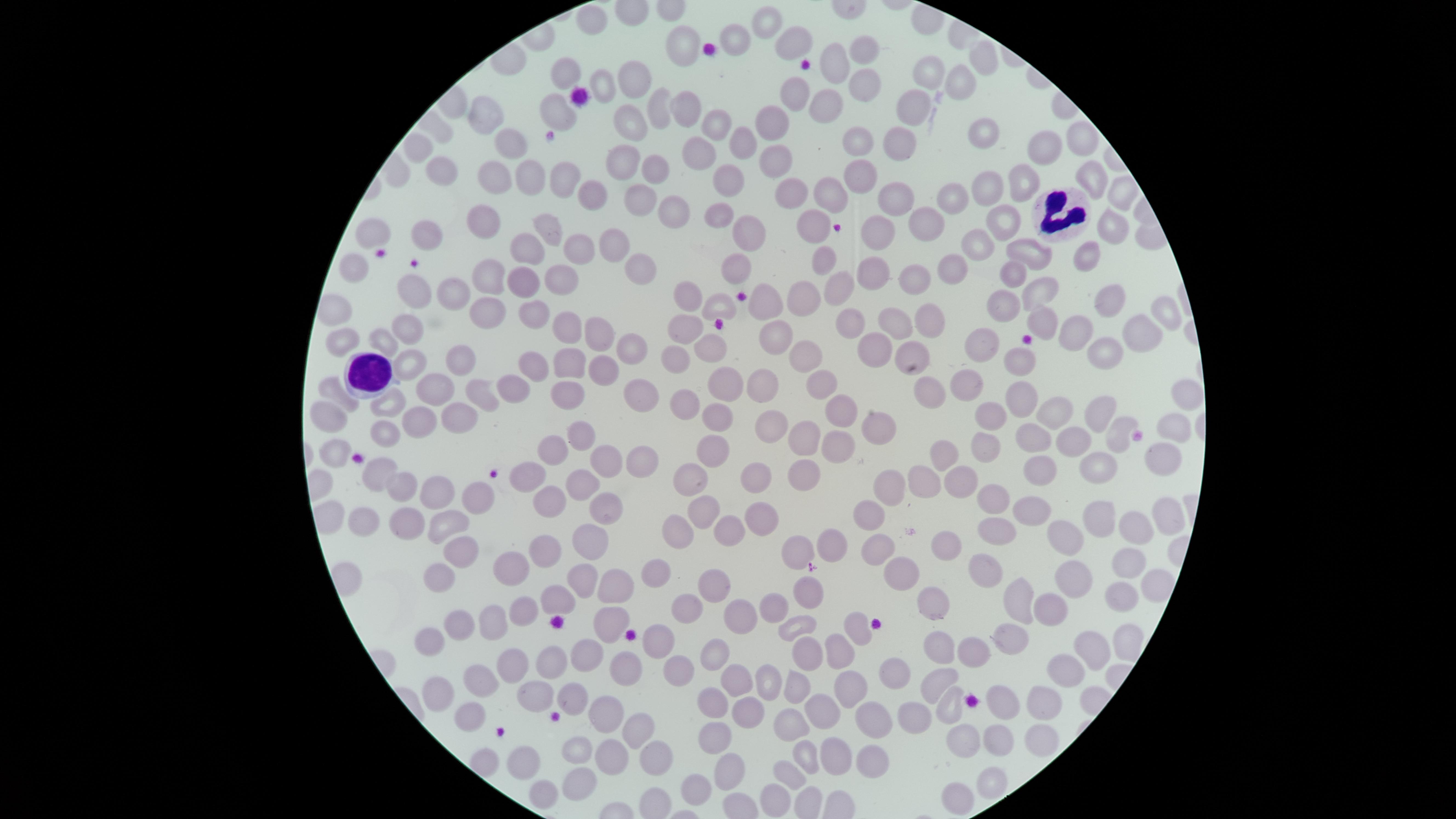
Approximate marker points as {x, y} in pixels. WBCs: {1062, 216}, {365, 371}. Uninfected RBCs: {593, 23}, {767, 26}, {736, 34}, {680, 40}, {793, 41}, {864, 44}, {983, 56}, {835, 63}, {564, 71}, {928, 74}, {633, 77}, {958, 80}, {863, 82}, {604, 87}, {793, 91}, {911, 102}, {658, 103}, {827, 106}, {684, 110}, {556, 113}, {490, 114}, {717, 122}, {774, 122}, {629, 124}, {982, 136}, {855, 137}, {511, 140}, {1078, 141}, {743, 143}, {896, 143}, {415, 146}, {700, 150}, {1042, 150}, {776, 160}, {619, 165}, {655, 171}, {439, 172}, {1087, 172}, {490, 174}, {855, 177}, {562, 179}, {729, 181}, {1023, 182}, {529, 185}, {794, 186}, {990, 187}, {831, 189}, {597, 190}, {899, 192}, {952, 192}, {1119, 194}, {638, 199}, {672, 214}, {718, 214}, {486, 215}, {999, 218}, {810, 222}, {927, 223}, {879, 226}, {1105, 227}, {550, 233}, {746, 233}, {375, 238}, {432, 238}, {975, 244}, {610, 246}, {524, 250}, {1028, 251}, {580, 252}, {824, 256}, {1086, 258}, {354, 266}, {734, 267}, {952, 267}, {876, 269}, {643, 270}, {1016, 271}, {559, 275}, {913, 276}, {489, 278}, {518, 278}, {839, 288}, {451, 289}, {408, 291}, {1035, 292}, {686, 293}, {800, 295}, {1114, 295}, {1005, 301}, {764, 304}, {718, 305}, {1165, 309}, {491, 312}, {531, 314}, {1043, 318}, {928, 319}, {849, 320}, {894, 324}, {683, 328}, {407, 329}, {1074, 330}, {569, 331}, {600, 331}, {1140, 331}, {778, 333}, {338, 338}, {386, 340}, {984, 342}, {1110, 343}, {707, 345}, {878, 346}, {637, 348}, {913, 348}, {807, 353}, {1020, 358}, {464, 360}, {537, 360}, {675, 360}, {408, 361}, {569, 363}, {606, 369}, {827, 378}, {967, 380}, {761, 382}, {730, 385}, {329, 387}, {437, 387}, {642, 388}, {927, 388}, {1019, 389}, {517, 390}, {480, 393}, {570, 393}, {1184, 393}, {682, 397}, {389, 400}, {1055, 410}, {1097, 411}, {990, 412}, {836, 416}, {323, 417}, {721, 417}, {461, 418}, {422, 419}, {770, 423}, {872, 424}, {1175, 425}, {380, 430}, {581, 432}, {1119, 433}, {810, 434}, {1066, 435}, {1027, 439}, {331, 445}, {987, 445}, {839, 446}, {548, 450}, {715, 452}, {942, 452}, {642, 453}, {1160, 457}, {606, 459}, {1100, 465}, {1044, 466}, {802, 473}, {955, 473}, {756, 476}, {693, 477}, {382, 478}, {533, 478}, {922, 484}, {581, 486}, {404, 488}, {894, 488}, {443, 496}, {985, 496}, {476, 500}, {701, 506}, {606, 507}, {551, 508}, {874, 510}, {1027, 510}, {753, 515}, {1163, 516}, {1098, 517}, {402, 520}, {360, 521}, {440, 522}, {1132, 527}, {990, 528}, {729, 531}, {676, 534}, {1069, 540}, {593, 542}, {949, 542}, {831, 543}, {879, 544}, {541, 551}, {794, 551}, {460, 553}, {1127, 561}, {512, 564}, {986, 565}, {902, 569}, {1077, 571}, {660, 573}, {442, 577}, {581, 581}, {1152, 585}, {618, 586}, {715, 590}, {1124, 592}, {810, 594}, {1015, 598}, {562, 601}, {934, 602}, {769, 605}, {1050, 606}, {689, 608}, {525, 609}, {608, 619}, {743, 619}, {497, 620}, {797, 623}, {462, 625}, {862, 627}, {1010, 631}, {436, 636}, {1124, 641}, {659, 644}, {942, 647}, {1091, 648}, {840, 652}, {976, 652}, {711, 653}, {804, 653}, {589, 656}, {544, 658}, {677, 666}, {508, 667}, {1066, 670}, {631, 672}, {894, 673}, {937, 677}, {733, 681}, {769, 682}, {479, 685}, {792, 686}, {852, 689}, {438, 691}, {539, 697}, {1003, 697}, {578, 698}, {709, 699}, {1037, 702}, {947, 706}, {604, 708}, {823, 709}, {745, 714}, {918, 714}, {468, 716}, {789, 719}, {869, 719}, {635, 723}, {966, 737}, {995, 739}, {1040, 739}, {719, 740}, {573, 746}, {654, 756}, {806, 756}, {613, 757}, {836, 757}, {871, 757}, {522, 758}, {730, 773}, {791, 774}, {989, 780}, {579, 781}, {543, 791}, {697, 793}, {961, 795}, {776, 798}. Circular visible region. Presence: no malaria parasites detected. Image is 1456×819 pixels. Giemsa stain. Single field of view. Thin smear of blood. Smartphone photograph through the microscope eyepiece.